Report the malaria status of this cell.
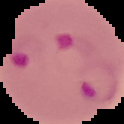
Parasitized.

Summary:
  - Image type: cell region segmented out of the field of view; surrounding area masked to black
  - Image size: 124×124 pixels
  - Preparation: thin blood film